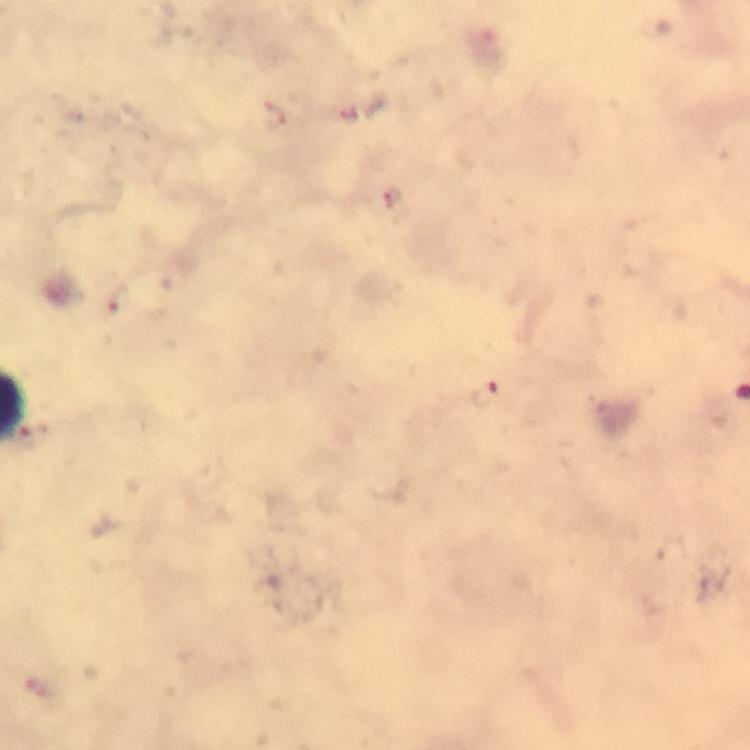

stain: Giemsa
image_size: 750×750 pixels
cropped_from: one field of view
preparation: thick blood smear
immersion_oil: applied
magnification: 100x
capture: smartphone camera through the microscope
malaria_parasite_locations: 'approximate centers as [x, y] in pixels: [394, 200], [116, 297], [487, 395]'
context: from a malaria diagnostic workup